State which parasite is depicted.
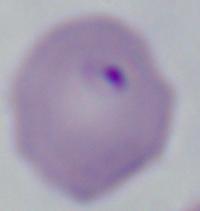

Babesia.

Summary:
  - Modality: micrograph
  - Magnification: 1000x